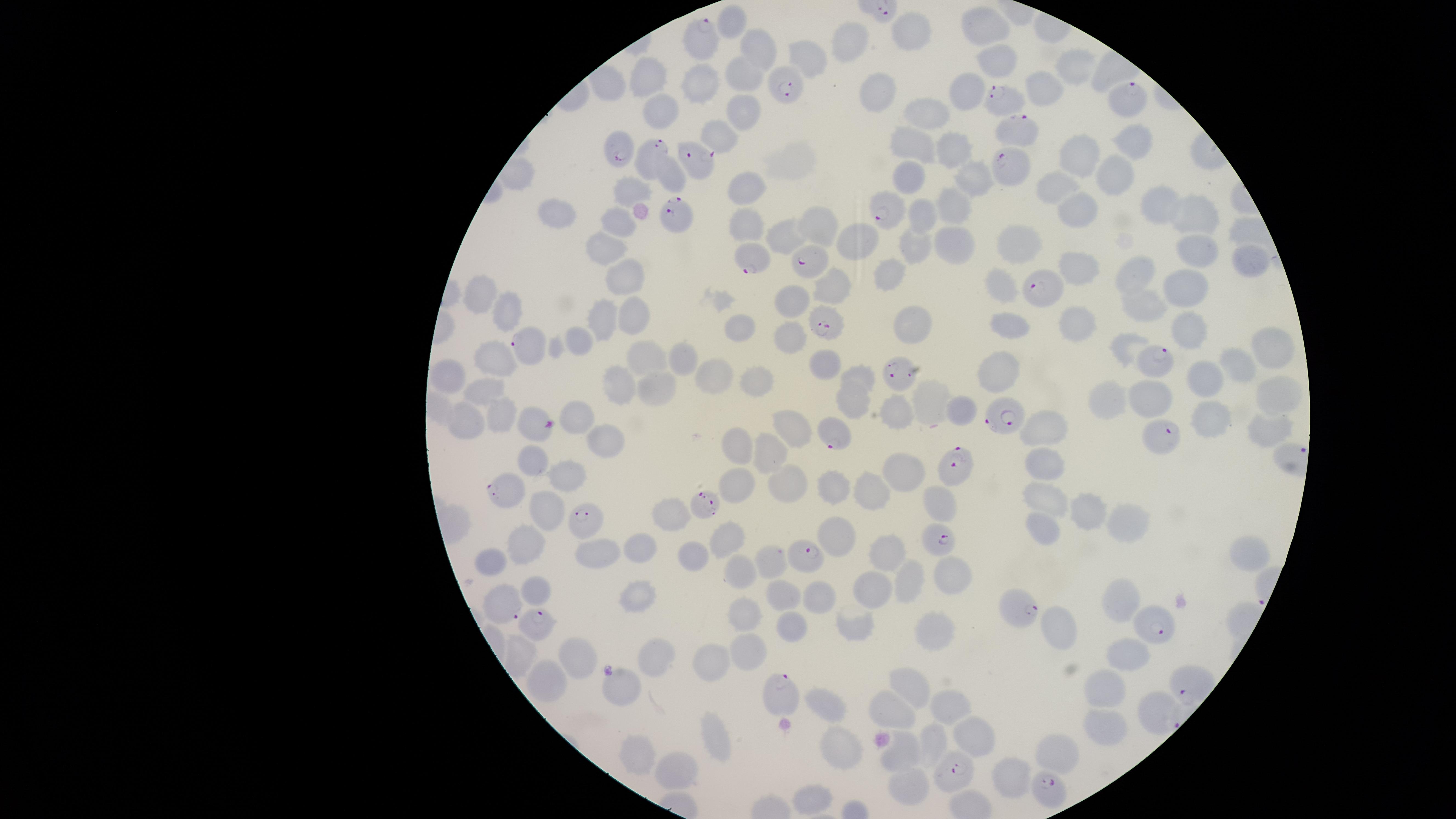

species = Plasmodium falciparum
visible region = circular
presence = malaria parasites identified
field of view = single
preparation = thin smear of blood
parasitized RBCs = approximate marker points as {x, y} in pixels: {698, 37}, {786, 83}, {1129, 98}, {1001, 99}, {1020, 132}, {607, 145}, {652, 152}, {697, 155}, {1011, 162}, {891, 207}, {673, 215}, {752, 259}, {804, 263}, {1044, 292}, {826, 321}, {531, 348}, {1155, 359}, {903, 372}, {1003, 417}, {543, 425}, {836, 431}, {1157, 436}, {954, 466}, {513, 485}, {705, 507}, {582, 517}, {942, 542}, {805, 560}, {504, 598}, {1014, 601}, {539, 618}, {1153, 626}, {780, 694}, {1155, 704}, {953, 771}, {1047, 789}
image size = 1456×819 pixels
uninfected RBCs = approximate marker points as {x, y} in pixels: {735, 17}, {914, 22}, {988, 26}, {846, 43}, {762, 48}, {997, 58}, {810, 59}, {746, 71}, {1077, 71}, {647, 79}, {705, 81}, {880, 85}, {1040, 86}, {969, 90}, {744, 98}, {925, 109}, {653, 112}, {719, 137}, {915, 142}, {1137, 143}, {957, 149}, {1080, 151}, {909, 174}, {1116, 175}, {975, 177}, {672, 179}, {632, 185}, {746, 189}, {1058, 190}, {947, 204}, {1158, 207}, {1076, 208}, {561, 210}, {1195, 216}, {617, 218}, {924, 218}, {744, 219}, {816, 227}, {856, 239}, {952, 240}, {1028, 240}, {787, 241}, {913, 246}, {603, 248}, {1194, 248}, {1246, 260}, {1078, 266}, {627, 270}, {1139, 270}, {889, 272}, {837, 287}, {1003, 287}, {1191, 289}, {483, 298}, {792, 300}, {1146, 302}, {603, 311}, {513, 312}, {636, 313}, {1072, 320}, {1008, 323}, {917, 325}, {743, 327}, {1189, 327}, {789, 333}, {581, 340}, {1124, 346}, {1272, 348}, {646, 357}, {818, 359}, {687, 361}, {493, 364}, {998, 365}, {1237, 368}, {719, 370}, {860, 373}, {451, 375}, {757, 379}, {619, 380}, {1204, 381}, {659, 385}, {483, 395}, {1275, 395}, {1111, 397}, {1158, 399}, {927, 403}, {857, 405}, {965, 410}, {1209, 410}, {503, 412}, {903, 412}, {578, 415}, {470, 421}, {1047, 422}, {1265, 423}, {795, 424}, {603, 438}, {734, 440}, {765, 443}, {535, 454}, {1048, 459}, {906, 470}, {569, 472}, {789, 480}, {837, 485}, {743, 486}, {876, 491}, {1047, 496}, {944, 501}, {1091, 509}, {665, 512}, {546, 513}, {1122, 522}, {840, 530}, {1038, 530}, {729, 538}, {523, 541}, {641, 546}, {891, 547}, {600, 552}, {693, 552}, {1243, 554}, {493, 557}, {773, 560}, {743, 569}, {952, 572}, {908, 581}, {867, 584}, {537, 585}, {1121, 596}, {641, 597}, {816, 599}, {780, 600}, {750, 612}, {854, 626}, {1062, 627}, {936, 629}, {789, 630}, {580, 647}, {657, 649}, {711, 650}, {752, 651}, {1132, 652}, {525, 654}, {550, 678}, {914, 681}, {1112, 688}, {622, 692}, {831, 702}, {956, 702}, {896, 707}, {1103, 721}, {970, 736}, {715, 738}, {931, 738}, {839, 743}, {638, 748}, {1059, 752}, {907, 754}, {674, 772}, {1011, 774}, {909, 783}, {814, 800}
capture = smartphone photograph through the microscope eyepiece
stain = Giemsa